Name the cell type shown.
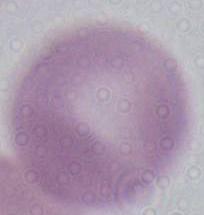
This is an erythrocyte.

{
  "magnification": "1000x",
  "modality": "micrograph"
}